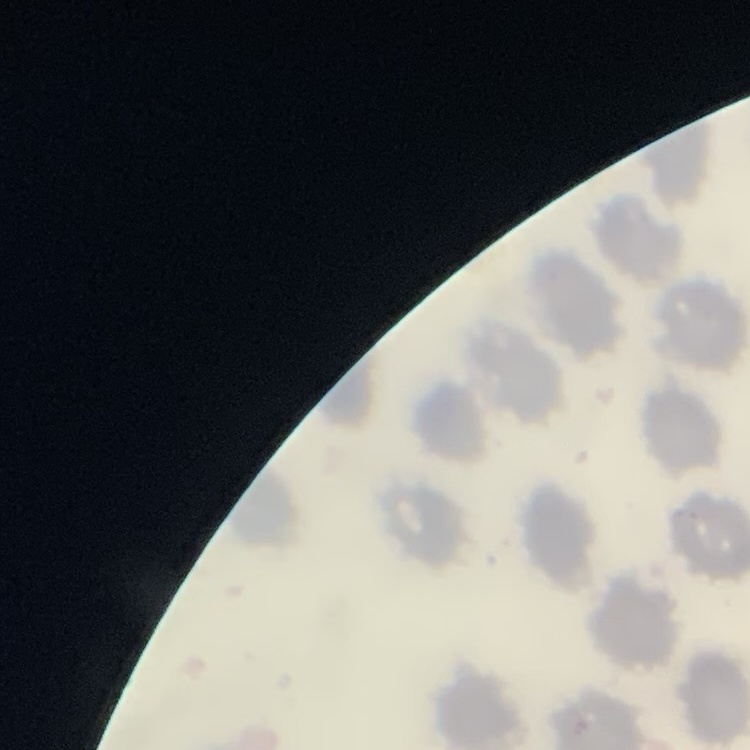

The erythrocytes show no rouleaux formation. One tile cut from a larger photomicrograph. Thin blood smear. Field's or Giemsa stain.